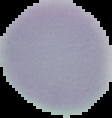 From a thin blood smear. Malaria status: uninfected. Image is 112×118 pixels. Cell region segmented out of the field of view; the surrounding area is masked to black.